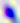 Toxoplasma gondii is seen. Micrograph. 400x magnification.